Report the malaria status of this cell.
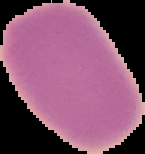

It is uninfected.

Summary:
  - Image size: 145×154 pixels
  - Preparation: thin blood film
  - Image type: cell region segmented out of the field of view; surrounding area masked to black